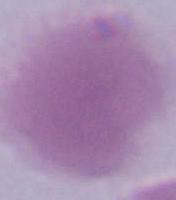

{
  "magnification": "1000x",
  "identification": "red blood cell",
  "modality": "photomicrograph"
}